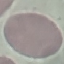

Summary:
  - Malaria status: uninfected
  - Image type: cell patch, automatically extracted from a larger field of view and resized to 64 × 64 pixels
  - Preparation: thin blood smear
  - Stain: Giemsa
  - Capture: smartphone camera at the microscope eyepiece